Locate every Plasmodium parasite.
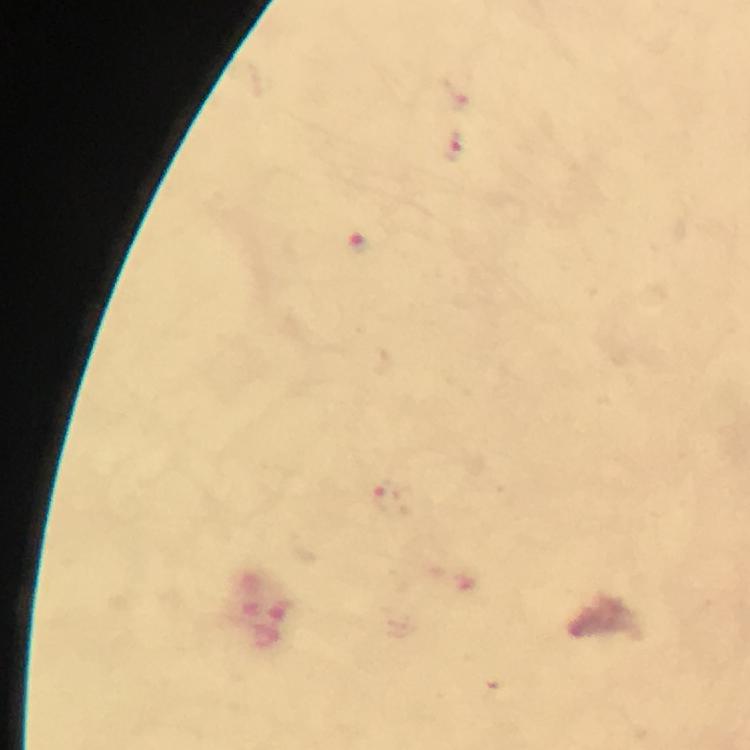

Approximate centers as [x, y] in pixels.
Plasmodium parasites: [455, 148], [362, 246], [388, 501].

Summary:
  - Context: from a diagnostic examination for malaria
  - Immersion oil: used
  - Capture: smartphone camera through the microscope
  - Image size: 750×750 pixels
  - Magnification: 100x
  - Cropped from: a single field of view
  - Preparation: thick blood smear
  - Stain: Giemsa